Report the malaria status of this cell.
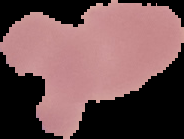
Uninfected.

Image is 184×139 pixels. From a thin blood smear. Cell region segmented out of the field of view; the surrounding area is masked to black.